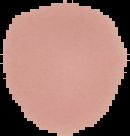

Summary:
  - Preparation: thin blood film
  - Malaria status: uninfected
  - Image size: 130×136 pixels
  - Image type: segmented cell region on a black background